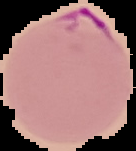
Summary:
  - Image size: 136×151 pixels
  - Result: malaria parasites identified
  - Preparation: thin blood smear
  - Image type: segmented cell region on a black background